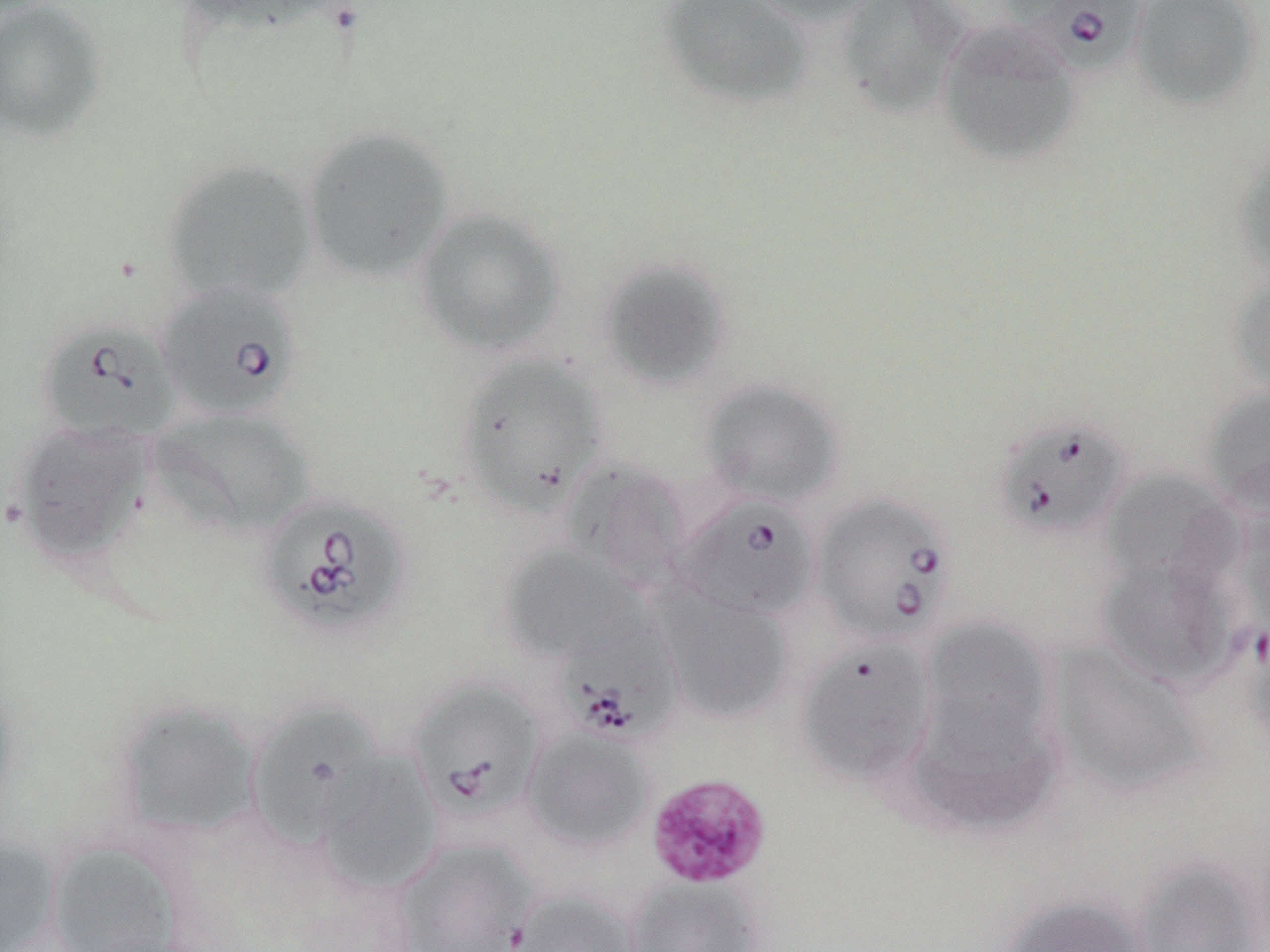

Summary:
  - Coordinate format: approximate bounding boxes as (x1, y1, x2, y2) in pixels
  - Platelet locations: (644, 772, 773, 890)
  - Uninfected red blood cell locations: (172, 0, 356, 39), (655, 0, 814, 111), (739, 0, 880, 27), (835, 0, 972, 119), (1129, 0, 1264, 112), (0, 1, 108, 143), (934, 19, 1082, 167), (300, 124, 455, 283), (1233, 146, 1270, 281), (161, 157, 319, 304), (413, 207, 566, 356), (596, 257, 732, 391), (1228, 268, 1270, 401), (454, 354, 608, 515), (699, 377, 847, 508), (1202, 386, 1270, 518), (148, 407, 316, 538), (12, 422, 152, 567), (562, 456, 691, 592), (1102, 470, 1240, 591), (501, 547, 648, 663), (1096, 557, 1240, 691), (654, 588, 795, 725), (920, 617, 1052, 751), (798, 638, 935, 787), (1046, 642, 1212, 800), (0, 681, 24, 823), (113, 699, 263, 840), (248, 706, 390, 855), (907, 707, 1061, 837), (521, 726, 657, 854), (317, 749, 441, 893), (0, 836, 63, 952), (392, 838, 539, 952), (44, 839, 188, 952), (1132, 856, 1266, 952), (624, 875, 764, 952), (506, 889, 643, 952), (997, 894, 1153, 952)
  - Babesia divergens-infected red blood cell locations: (1007, 0, 1152, 77), (154, 280, 304, 421), (36, 318, 181, 445), (993, 415, 1132, 541), (811, 491, 957, 648), (255, 493, 411, 638), (672, 493, 819, 621), (552, 617, 683, 747), (409, 678, 545, 824)
  - Slide-level diagnosis: Babesia divergens
  - Modality: light microscopy
  - Field of view: single
  - Stain: May-Grünwald-Giemsa
  - Preparation: thin blood film
  - Magnification: 1000x
  - Image size: 1270×952 pixels